Classify this cell by malaria status.
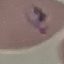
Parasitized.

image type = cell patch, automatically extracted from a larger field of view and resized to 64 × 64 pixels
preparation = thin blood film
capture = smartphone through the microscope eyepiece
stain = Giemsa